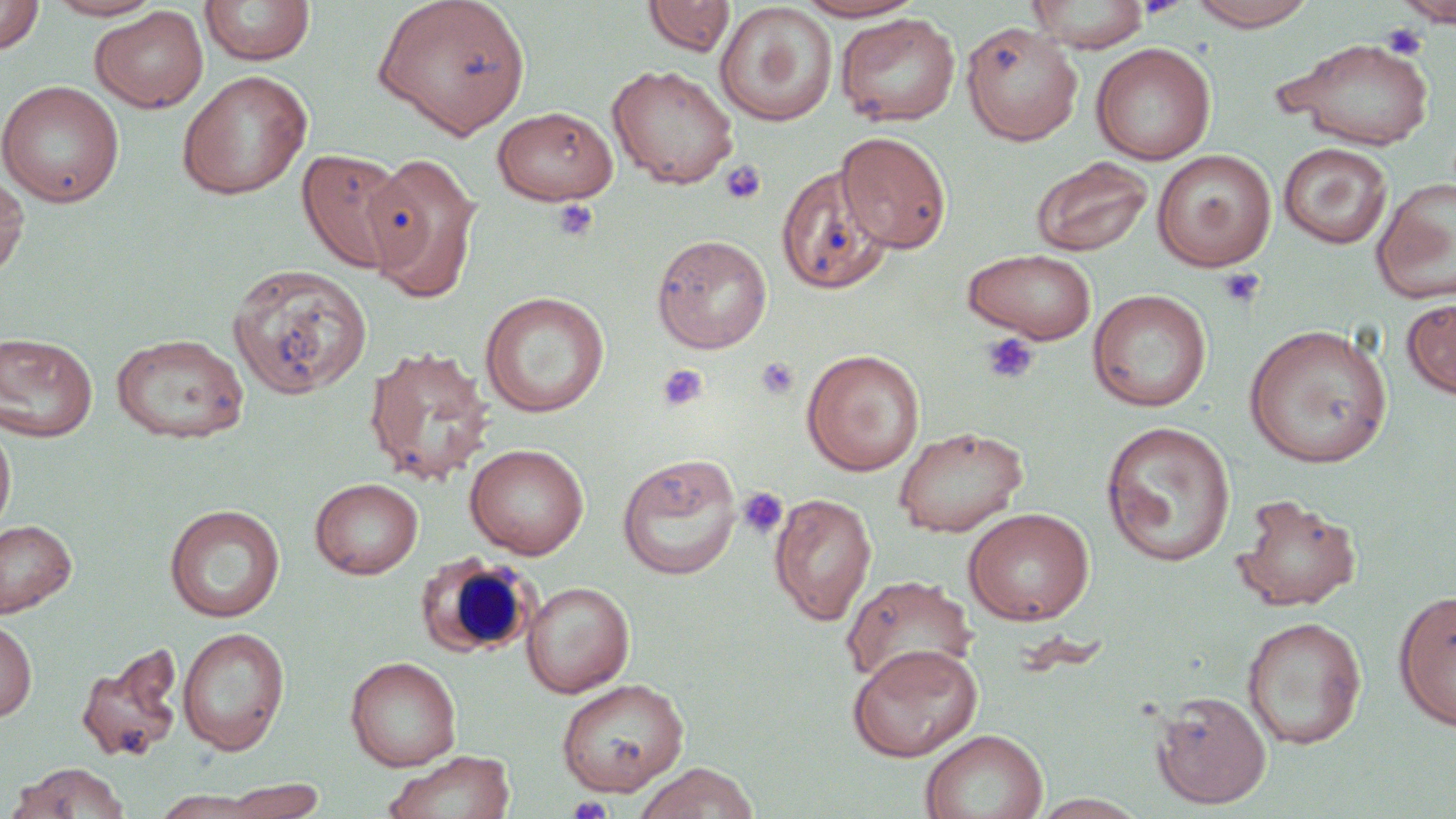 Approximate bounding boxes as (x1, y1, x2, y2) in pixels. Platelet locations: (1395, 0, 1456, 27), (1379, 22, 1428, 60), (720, 160, 767, 205), (551, 199, 599, 242), (1217, 267, 1266, 310), (981, 332, 1040, 385), (756, 356, 800, 401), (657, 364, 708, 410), (737, 487, 789, 540), (568, 796, 612, 819). White blood cell locations: (415, 553, 537, 659). Uninfected red blood cell locations: (0, 0, 45, 55), (43, 0, 166, 20), (374, 0, 530, 139), (643, 0, 736, 57), (792, 0, 928, 22), (1025, 0, 1151, 53), (1186, 0, 1319, 31), (1394, 0, 1456, 28), (199, 1, 316, 66), (715, 2, 839, 126), (90, 6, 209, 113), (835, 13, 960, 127), (961, 21, 1083, 145), (1277, 38, 1437, 149), (1090, 42, 1217, 165), (607, 63, 739, 189), (177, 70, 313, 200), (0, 80, 124, 208), (491, 106, 618, 205), (836, 137, 952, 258), (1278, 142, 1393, 249), (296, 148, 410, 274), (1152, 149, 1276, 273), (364, 152, 483, 302), (1030, 157, 1153, 258), (776, 166, 891, 294), (0, 168, 30, 281), (1371, 178, 1456, 304), (651, 233, 773, 354), (963, 248, 1098, 344), (227, 263, 372, 399), (1087, 289, 1212, 412), (480, 291, 610, 417), (1401, 297, 1456, 400), (1244, 323, 1392, 468), (0, 332, 98, 442), (110, 333, 249, 444), (364, 346, 495, 485), (801, 348, 925, 475), (0, 421, 17, 538), (1100, 421, 1236, 566), (893, 425, 1029, 537), (464, 443, 589, 559), (617, 453, 742, 580), (310, 477, 423, 579), (769, 492, 877, 626), (1231, 493, 1362, 611), (164, 504, 285, 622), (963, 507, 1094, 625), (0, 518, 77, 618), (841, 574, 977, 689), (521, 581, 634, 697), (1393, 589, 1456, 731), (1241, 616, 1366, 749), (0, 617, 37, 722), (177, 626, 290, 756), (847, 643, 982, 762), (75, 644, 184, 763), (345, 655, 462, 771), (556, 677, 688, 797), (1149, 690, 1273, 809), (921, 728, 1047, 819), (385, 749, 516, 819), (12, 762, 131, 818), (634, 762, 760, 819), (207, 778, 331, 819), (149, 789, 278, 818), (1030, 793, 1150, 818). Slide-level diagnosis: negative for blood parasites. 1000x magnification. May-Grünwald-Giemsa stain. Thin blood film. Light microscopy. Image is 1456×819 pixels. Single field of view.